Classify this cell by malaria status.
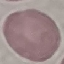

Uninfected.

Giemsa stain. Cell patch, automatically extracted from a larger field of view and resized to 64 × 64 pixels. Acquired by smartphone through the microscope eyepiece. Thin smear of blood.